Locate every malaria parasite.
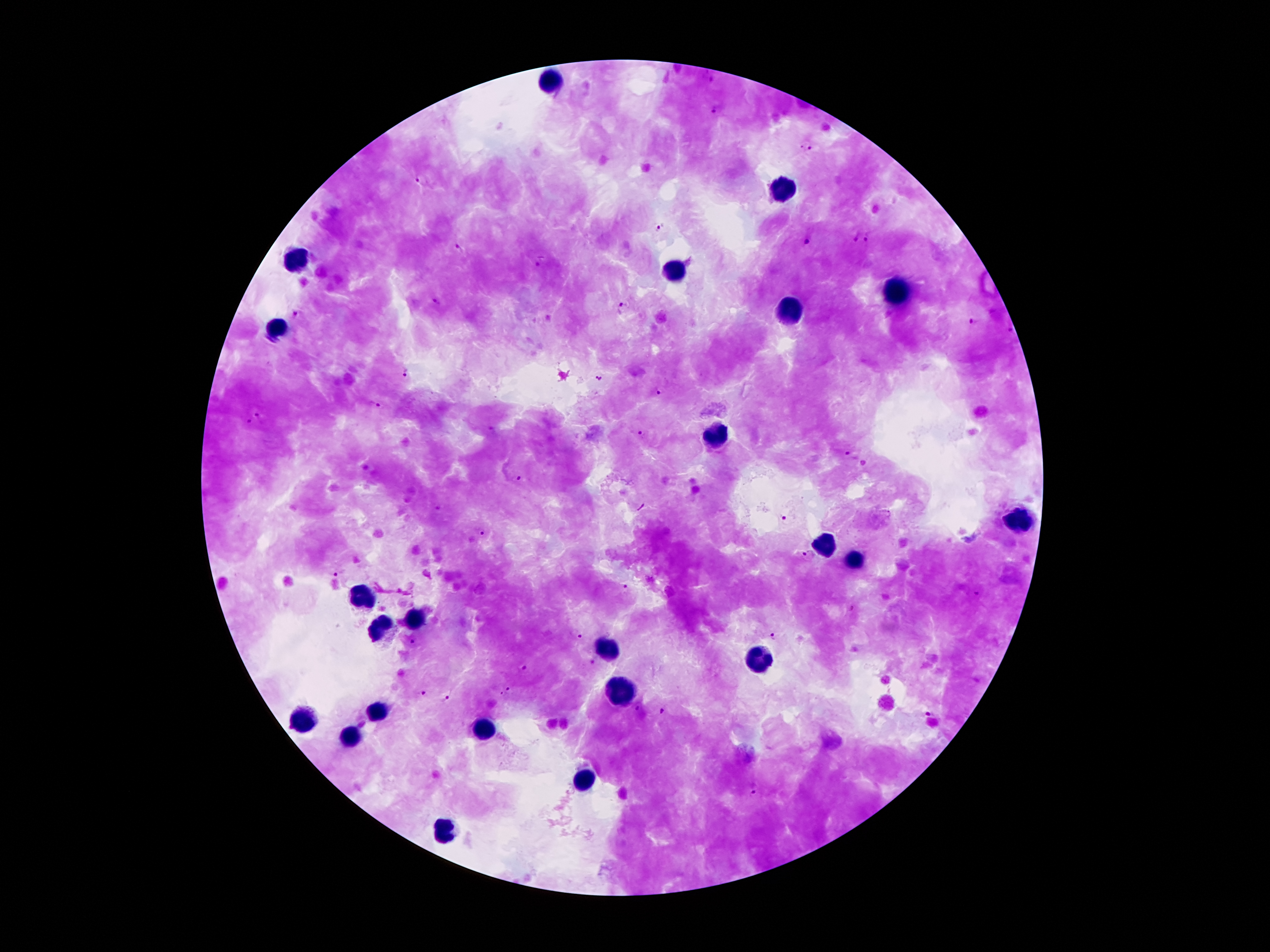
Approximate object centers, in pixels from the top-left corner.
Malaria parasites: (x=715, y=111), (x=805, y=146), (x=420, y=180), (x=656, y=228), (x=868, y=239), (x=807, y=242), (x=458, y=249), (x=434, y=301), (x=621, y=308), (x=295, y=312), (x=973, y=322), (x=408, y=372), (x=599, y=378), (x=661, y=391), (x=376, y=406), (x=261, y=416), (x=247, y=422), (x=642, y=435), (x=847, y=453), (x=518, y=478), (x=783, y=519), (x=479, y=530), (x=807, y=557), (x=338, y=574), (x=623, y=587), (x=976, y=594), (x=850, y=609), (x=576, y=635), (x=772, y=637), (x=414, y=643), (x=593, y=661), (x=521, y=667), (x=420, y=690), (x=504, y=690), (x=446, y=698), (x=636, y=709), (x=662, y=710), (x=928, y=713), (x=754, y=795).

preparation: thick peripheral-blood smear
capture: smartphone through the microscope eyepiece
leukocyte_locations: 'approximate object centers, in pixels from the top-left corner: (x=551, y=81), (x=782, y=187), (x=296, y=261), (x=673, y=272), (x=895, y=290), (x=789, y=312), (x=277, y=328), (x=714, y=436), (x=1015, y=519), (x=823, y=542), (x=858, y=561), (x=363, y=598), (x=413, y=617), (x=378, y=629), (x=611, y=646), (x=756, y=662), (x=621, y=690), (x=378, y=710), (x=303, y=721), (x=481, y=727), (x=349, y=737), (x=585, y=782), (x=444, y=831)'
magnification: 100x
image_size: 1270×952 pixels
field_of_view: single
patient_malaria_status: infected with Plasmodium falciparum
stain: Giemsa